Assess this cell for malaria.
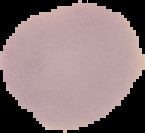

It is uninfected.

image size = 145×133 pixels
preparation = thin blood film
image type = segmented cell region on a black background